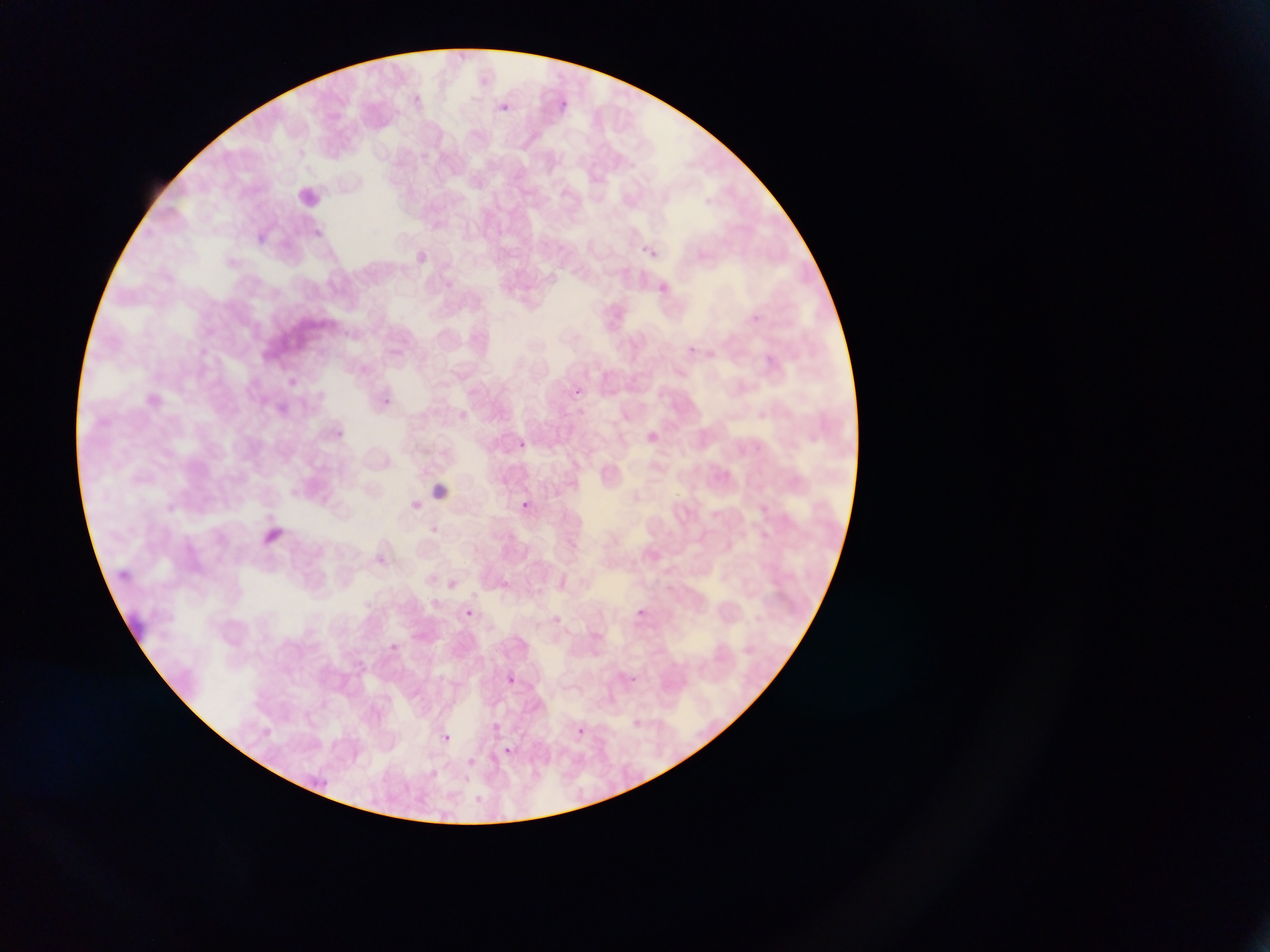 Approximate bounding boxes as {left, top, right, bottom} in pixels. Leukocyte locations: {430, 480, 459, 502}. Plasmodium parasite locations: {554, 91, 573, 120}, {498, 98, 510, 115}, {408, 244, 438, 277}, {640, 244, 671, 267}, {689, 345, 700, 360}, {573, 388, 606, 414}, {376, 394, 396, 411}, {333, 429, 356, 449}, {513, 438, 529, 451}, {513, 497, 535, 515}, {634, 607, 650, 621}, {464, 609, 473, 618}, {390, 643, 402, 652}, {502, 672, 520, 688}, {630, 673, 648, 689}, {572, 723, 589, 739}, {433, 730, 455, 749}, {496, 743, 517, 762}. Thin blood smear. Mobile-phone photograph taken through the microscope. Image is 1270×952 pixels. Collected in Ghana. Single field of view.